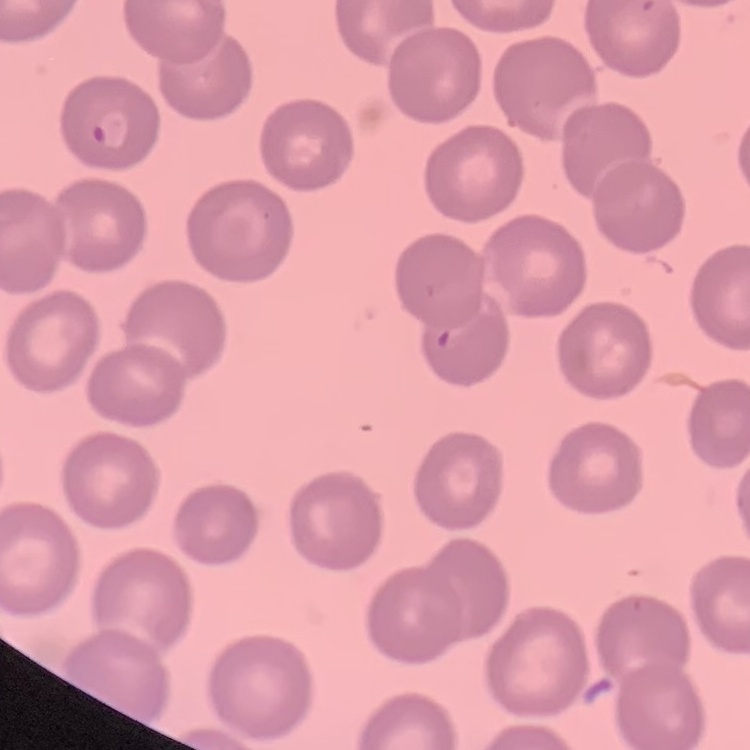
red_blood_cell_morphology: no rouleaux formation
image_type: one tile cut from a larger photomicrograph
stain: Field's or Giemsa
preparation: thin peripheral smear